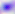
Photomicrograph. Toxoplasma gondii is shown. 400x magnification.